Give the extent of all Plasmodium falciparum-infected red blood cells.
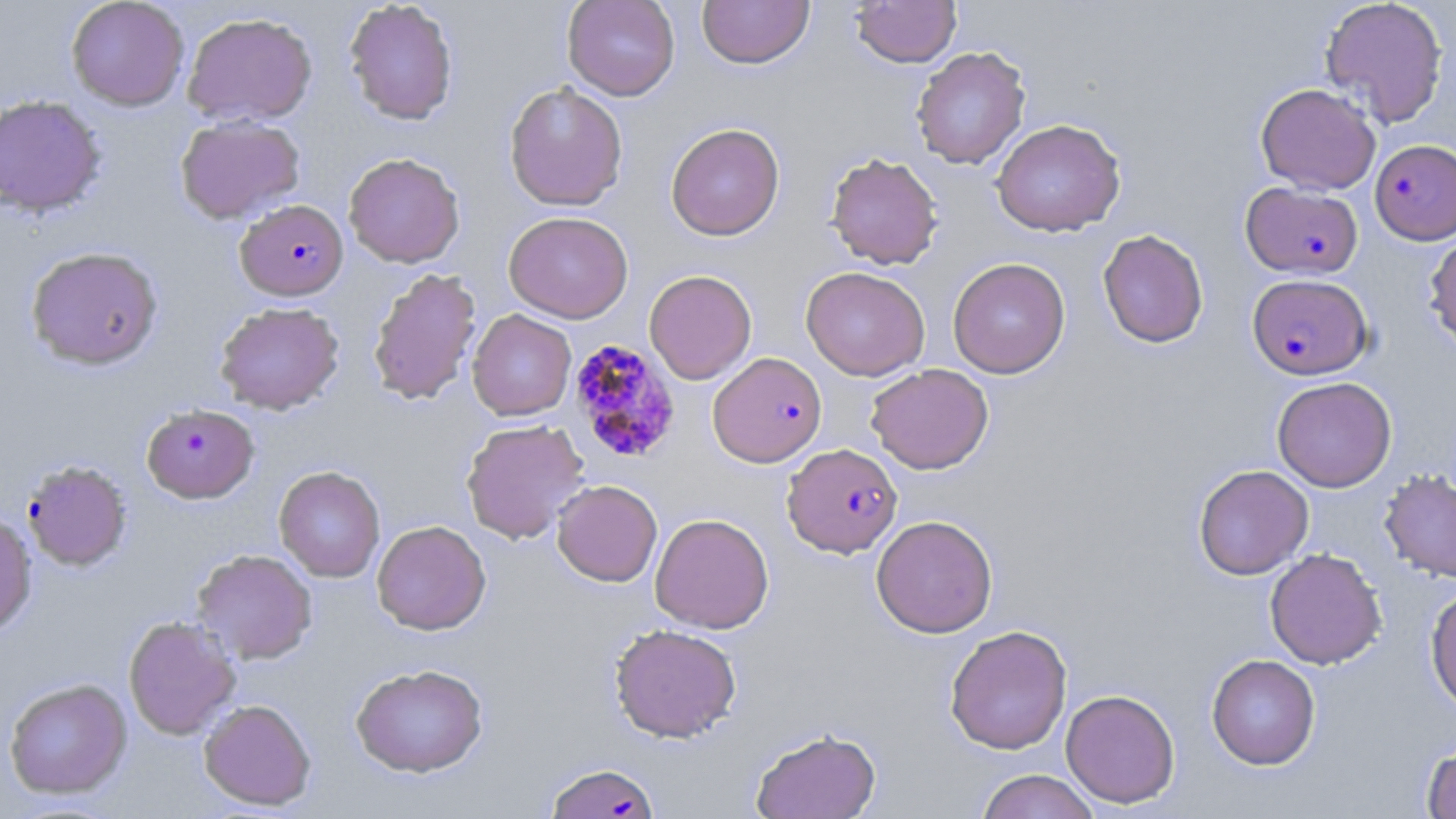

Approximate bounding boxes as (x1,y1)-(x2,y2) corner pairs in pixels.
Plasmodium falciparum-infected red blood cells: (1371,138)-(1456,245), (1241,182)-(1363,278), (235,199)-(349,300), (1247,274)-(1372,379), (568,338)-(683,464), (707,351)-(827,468), (140,403)-(260,503), (782,442)-(903,558), (21,459)-(133,571), (545,762)-(660,818).

{
  "slide_level_diagnosis": "Plasmodium falciparum",
  "image_size": "1456×819 pixels",
  "uninfected_red_blood_cell_locations": "approximate bounding boxes as (x1,y1)-(x2,y2) corner pairs in pixels: (66,0)-(189,111), (562,0)-(680,101), (697,0)-(814,69), (851,0)-(961,67), (1319,0)-(1449,129), (344,1)-(458,125), (182,12)-(318,127), (911,46)-(1031,169), (504,81)-(628,212), (1255,83)-(1381,194), (0,94)-(107,217), (175,115)-(305,224), (991,118)-(1126,236), (665,122)-(785,241), (343,152)-(465,268), (825,152)-(943,269), (504,211)-(633,323), (1097,228)-(1209,348), (1424,229)-(1456,352), (25,246)-(164,370), (947,257)-(1071,379), (801,266)-(930,381), (367,267)-(482,406), (644,269)-(757,385), (214,301)-(344,415), (467,309)-(576,421), (866,363)-(993,475), (1272,376)-(1397,492), (461,418)-(591,544), (1193,464)-(1313,580), (273,465)-(385,582), (1379,468)-(1456,584), (552,479)-(663,586), (0,511)-(33,637), (650,513)-(774,634), (871,514)-(998,638), (372,520)-(491,635), (1264,548)-(1387,669), (191,549)-(317,665), (1425,584)-(1456,713), (123,615)-(241,740), (608,623)-(742,743), (944,624)-(1072,755), (1206,654)-(1321,770), (350,664)-(488,778), (3,678)-(133,800), (1060,689)-(1181,808), (199,698)-(316,811), (750,727)-(881,819), (1421,740)-(1455,819), (976,769)-(1100,819)",
  "field_of_view": "single",
  "modality": "optical microscopy",
  "preparation": "thin blood smear",
  "magnification": "1000x",
  "stain": "May-Grünwald-Giemsa"
}